Give a bounding box for every trophozoite.
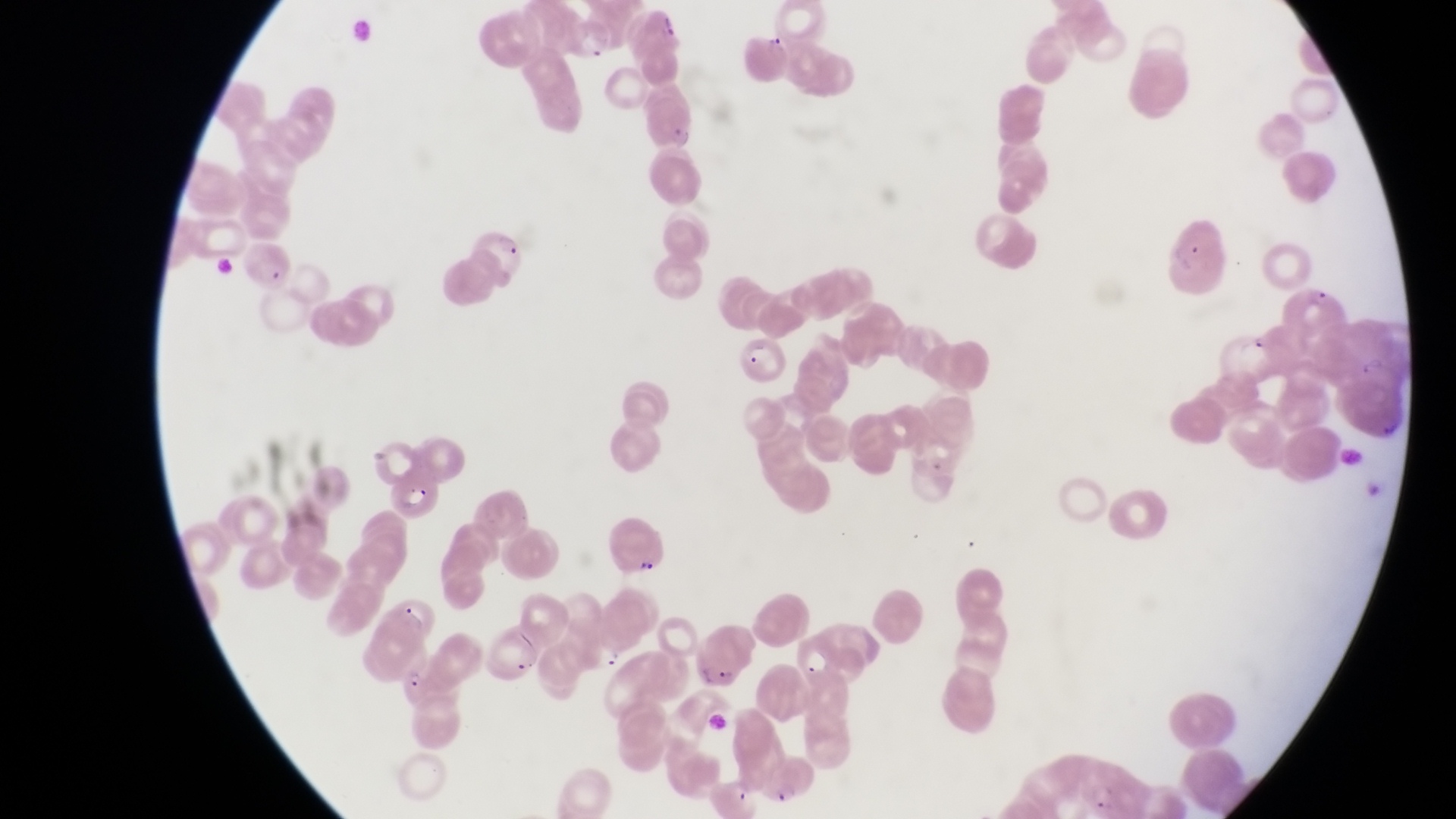

Approximate bounding boxes as (left, top, right, bottom) in pixels.
Trophozoites: (597, 647, 624, 670).

Parasitised red blood cell locations: (566, 21, 618, 60), (645, 99, 708, 155), (1160, 206, 1227, 289), (469, 225, 529, 286), (240, 238, 293, 284), (1287, 278, 1347, 341), (736, 333, 789, 382), (388, 468, 444, 517), (693, 627, 756, 691), (796, 632, 848, 688), (400, 658, 472, 714). Artifact (platelet-like body, stain precipitate, or debris) locations: (639, 560, 660, 579), (515, 654, 536, 678). Magnification of 1000x. Thin blood film. Sample from Uganda. Image is 1456×819 pixels. One field of view. Captured by a smartphone held over the eyepiece of an Olympus CX-23 microscope.